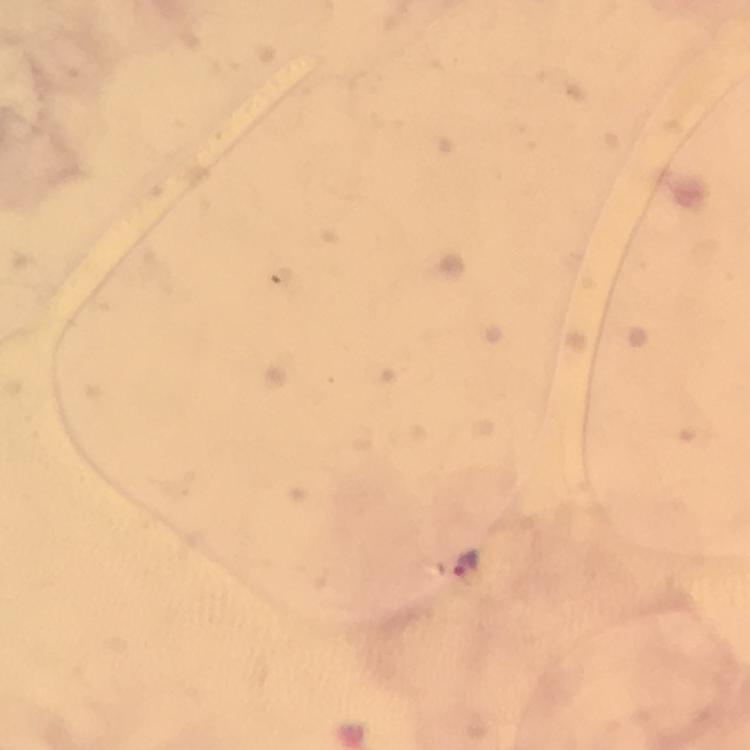
Approximate centers as [x, y] in pixels. Malaria parasite locations: [468, 564]. Giemsa stain. From a malaria diagnostic workup. At 100x magnification. Photographed through the microscope with a smartphone camera. Immersion oil was used. Thick blood film. Image is 750×750 pixels. A crop from one field of view.